Classify this cell by malaria status.
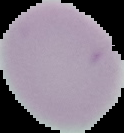

It is uninfected.

Summary:
  - Preparation: thin blood smear
  - Image size: 124×133 pixels
  - Image type: segmented cell region on a black background